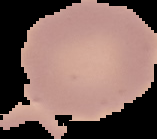

{
  "image_type": "cell region segmented out of the field of view; surrounding area masked to black",
  "malaria_status": "uninfected",
  "preparation": "thin blood film",
  "image_size": "157×139 pixels"
}